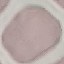

Malaria status: uninfected. Automatically extracted cell patch, resized to 64 × 64 pixels. Acquired by smartphone through the microscope eyepiece. Thin blood film. Giemsa-stained preparation.